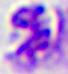
Summary:
  - Identification: white blood cell
  - Magnification: 400x
  - Modality: micrograph